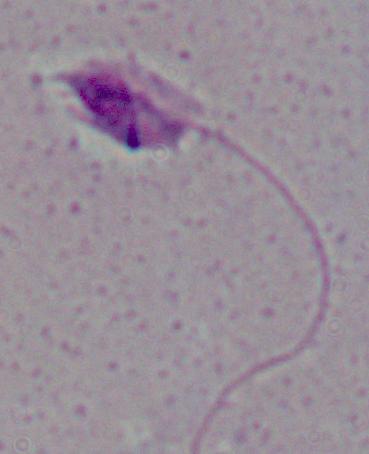

A Leishmania parasite is seen. Captured at 1000x magnification. Photomicrograph.